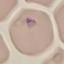
Summary:
  - Result: no malaria parasites seen
  - Stain: Giemsa
  - Capture: smartphone camera at the microscope eyepiece
  - Preparation: thin blood smear
  - Image type: cell patch, automatically extracted from a larger field of view and resized to 64 × 64 pixels